Classify this cell by malaria status.
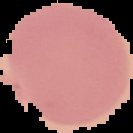
Uninfected.

Summary:
  - Preparation: thin blood film
  - Image type: segmented cell region on a black background
  - Image size: 133×133 pixels